Locate every leukocyte (white blood cell).
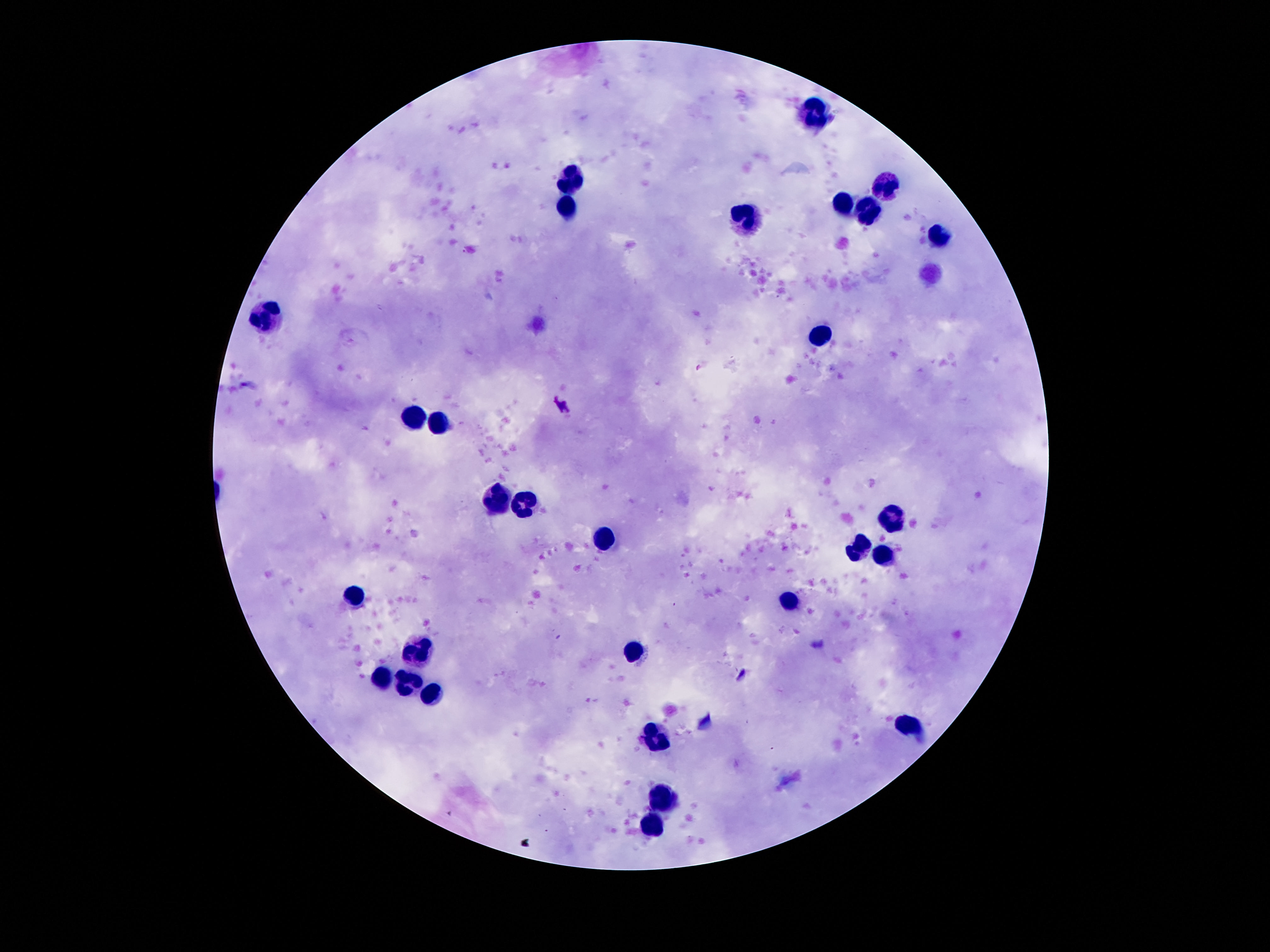
Approximate object centers, in pixels from the top-left corner.
Leukocytes: (x=811, y=111), (x=570, y=178), (x=884, y=188), (x=844, y=201), (x=564, y=208), (x=869, y=212), (x=744, y=219), (x=940, y=234), (x=266, y=314), (x=820, y=337), (x=415, y=417), (x=437, y=423), (x=493, y=497), (x=521, y=501), (x=891, y=522), (x=600, y=540), (x=857, y=550), (x=882, y=557), (x=353, y=593), (x=788, y=600), (x=421, y=647), (x=635, y=649), (x=381, y=677), (x=408, y=684), (x=430, y=692), (x=908, y=726), (x=660, y=738), (x=665, y=793), (x=652, y=823).

magnification: 100x
preparation: thick peripheral-blood smear
field_of_view: single
stain: Giemsa
patient_malaria_status: negative
capture: smartphone camera through the microscope eyepiece
image_size: 1270×952 pixels